Identify the parasite.
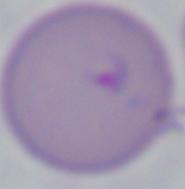
This is Babesia.

1000x magnification. Photomicrograph.